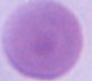
Summary:
  - Modality: photomicrograph
  - Magnification: 1000x
  - Identification: erythrocyte